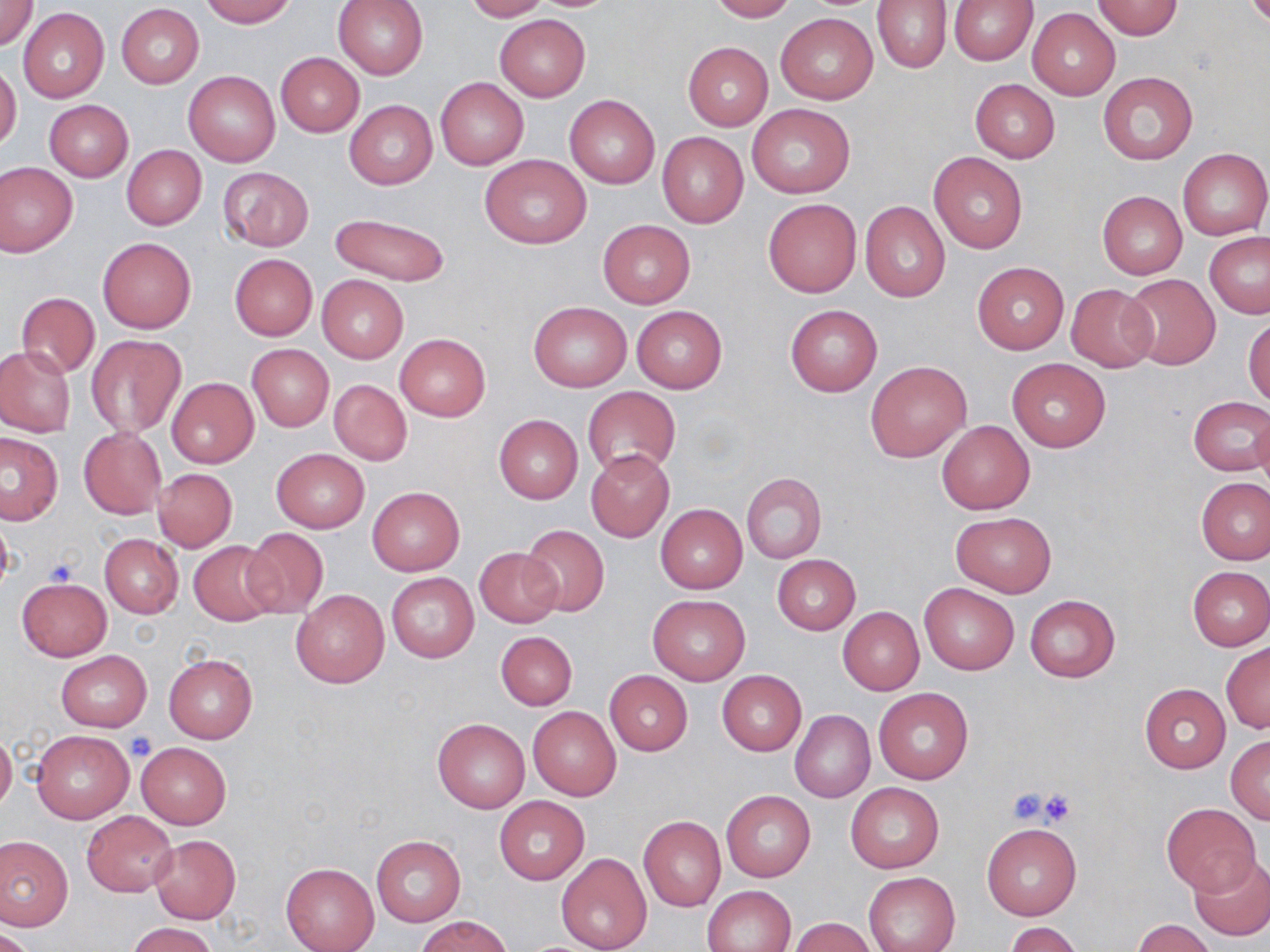 Approximate bounding boxes as [x1, y1, x2, y2] in pixels. Platelet locations: [42, 557, 78, 590], [126, 732, 156, 761], [1005, 787, 1053, 827], [1037, 788, 1080, 825]. Uninfected red blood cell locations: [199, 0, 297, 27], [333, 0, 427, 80], [462, 0, 551, 21], [707, 0, 797, 21], [872, 0, 952, 73], [948, 0, 1038, 64], [0, 1, 39, 50], [1092, 1, 1183, 39], [117, 4, 203, 88], [1027, 7, 1121, 99], [18, 8, 109, 103], [776, 13, 877, 104], [495, 15, 590, 102], [682, 42, 774, 130], [276, 52, 363, 136], [0, 62, 21, 152], [182, 70, 280, 166], [1097, 71, 1197, 165], [435, 78, 527, 169], [970, 79, 1060, 163], [564, 95, 660, 189], [44, 100, 134, 181], [344, 100, 437, 189], [746, 103, 854, 198], [656, 131, 748, 228], [121, 145, 206, 230], [1178, 148, 1270, 240], [928, 151, 1028, 254], [479, 154, 591, 249], [1, 162, 78, 258], [218, 167, 314, 251], [1098, 191, 1187, 279], [763, 199, 861, 298], [860, 201, 950, 301], [328, 212, 450, 288], [598, 219, 695, 308], [1204, 232, 1270, 318], [98, 237, 196, 333], [229, 254, 317, 341], [971, 262, 1069, 354], [318, 274, 408, 363], [1118, 274, 1222, 370], [1066, 283, 1158, 372], [15, 294, 100, 376], [528, 302, 632, 391], [784, 304, 882, 396], [631, 306, 727, 392], [1244, 315, 1270, 406], [85, 334, 185, 439], [394, 334, 490, 421], [247, 344, 333, 431], [0, 345, 76, 437], [1006, 357, 1110, 452], [867, 360, 971, 461], [166, 377, 258, 468], [328, 379, 412, 466], [583, 386, 681, 479], [1187, 396, 1270, 476], [1251, 409, 1270, 503], [494, 415, 582, 504], [937, 419, 1035, 514], [79, 428, 165, 519], [0, 432, 63, 525], [271, 448, 369, 533], [586, 450, 675, 541], [154, 468, 237, 552], [740, 472, 827, 564], [1197, 478, 1270, 565], [367, 486, 464, 575], [656, 503, 747, 594], [1, 512, 14, 597], [951, 512, 1057, 596], [520, 524, 611, 617], [239, 529, 328, 619], [100, 534, 182, 617], [189, 540, 281, 626], [474, 547, 565, 628], [772, 555, 860, 635], [1187, 566, 1270, 650], [387, 573, 478, 663], [17, 579, 110, 660], [919, 583, 1019, 675], [291, 588, 390, 688], [648, 594, 749, 685], [1024, 595, 1120, 682], [838, 607, 924, 695], [496, 631, 577, 710], [1221, 643, 1270, 733], [55, 650, 152, 732], [164, 654, 258, 742], [604, 670, 693, 755], [718, 671, 806, 755], [1139, 684, 1231, 772], [873, 687, 973, 785], [528, 706, 622, 801], [790, 710, 875, 802], [432, 717, 529, 813], [32, 730, 134, 823], [0, 732, 16, 812], [1226, 736, 1270, 823], [136, 742, 230, 828], [845, 782, 944, 874], [721, 789, 815, 882], [495, 797, 588, 884], [1161, 802, 1261, 895], [82, 811, 177, 896], [639, 815, 726, 912], [982, 823, 1081, 919], [0, 835, 72, 931], [149, 835, 240, 923], [371, 835, 465, 926], [556, 853, 651, 952], [1188, 854, 1270, 940], [281, 862, 379, 952], [863, 871, 960, 952], [704, 886, 796, 952], [418, 915, 513, 952], [788, 918, 878, 951], [1133, 920, 1216, 952], [125, 922, 218, 952], [1007, 922, 1083, 952], [1, 927, 38, 952]. Slide-level diagnosis: negative for blood parasites. Light microscopy. 1000x magnification. Thin blood film. Image is 1270×952 pixels. May-Grünwald-Giemsa stain. Single field of view.